Describe the morphology of the erythrocytes.
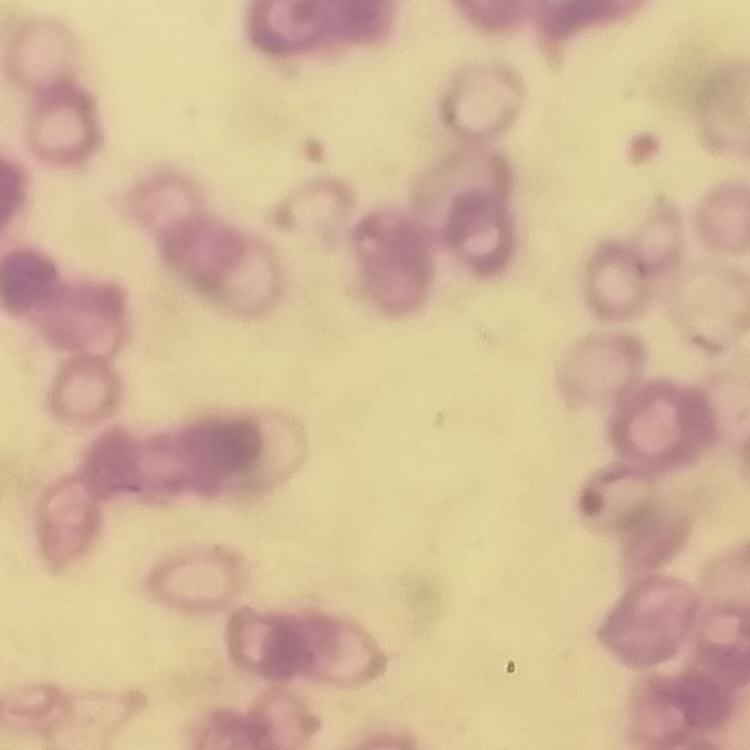

They show rouleaux formation.

Summary:
  - Preparation: thin blood film
  - Image type: one tile cut from a larger photomicrograph
  - Stain: Field's or Giemsa